Assess this cell for malaria.
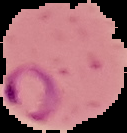
It is parasitized.

Summary:
  - Preparation: thin blood smear
  - Image size: 127×133 pixels
  - Image type: segmented cell region on a black background